Assess the morphology of the erythrocytes.
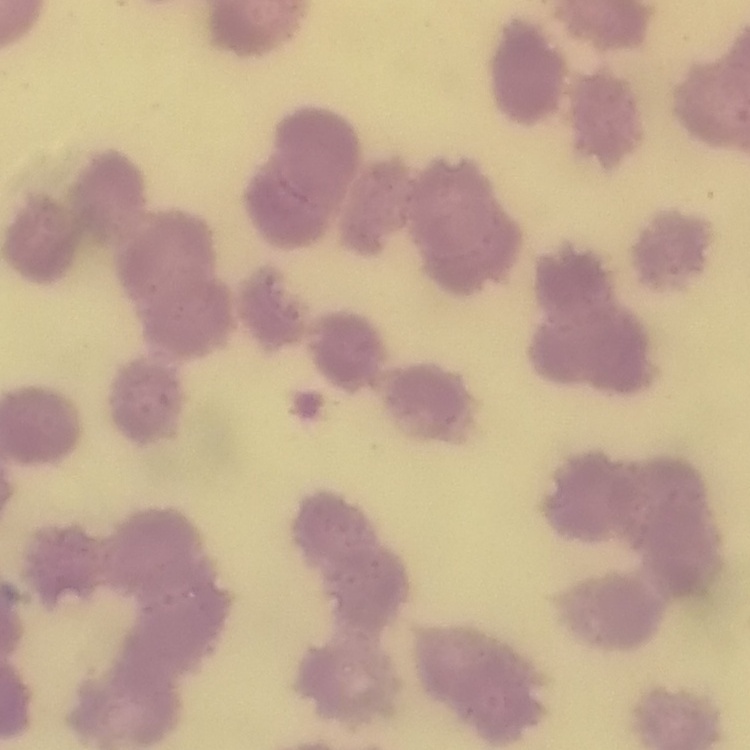
They show rouleaux formation.

Field's or Giemsa stain. One tile cut from a larger photomicrograph. Thin blood film.